Assess the morphology of the erythrocytes.
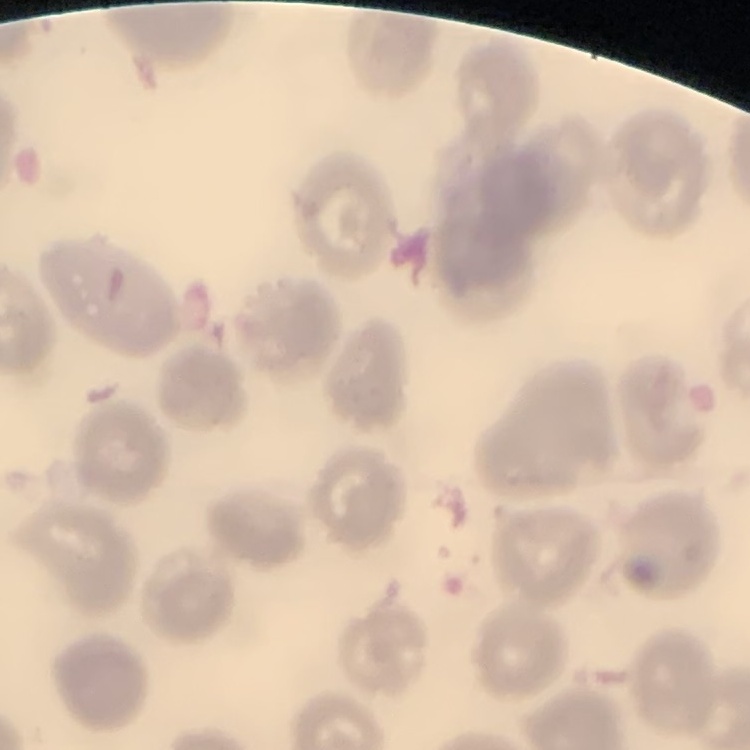
They show no rouleaux formation.

Stained with either Field's or Giemsa. Square crop of a larger photomicrograph. Thin blood film.